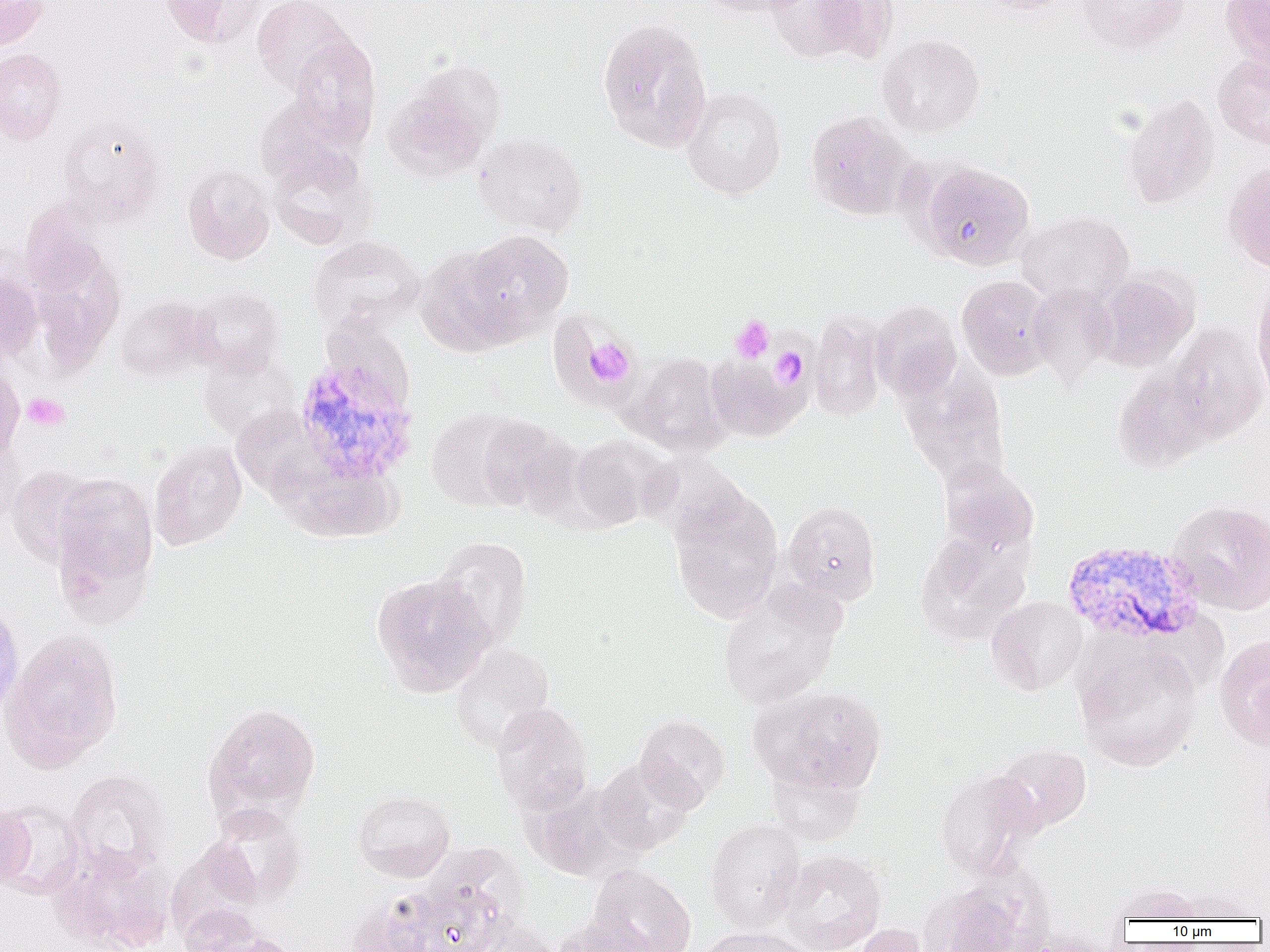
Summary:
  - Coordinate format: approximate bounding boxes as named x1/y1/x2/y2 corners in pixels
  - Plasmodium vivax-infected red blood cell locations: (x1=292, y1=354, x2=418, y2=486), (x1=1061, y1=540, x2=1205, y2=646)
  - Uninfected red blood cell locations: (x1=0, y1=0, x2=50, y2=51), (x1=158, y1=0, x2=265, y2=48), (x1=251, y1=0, x2=356, y2=93), (x1=695, y1=0, x2=810, y2=17), (x1=767, y1=0, x2=885, y2=62), (x1=978, y1=0, x2=1071, y2=14), (x1=1078, y1=0, x2=1189, y2=52), (x1=1220, y1=0, x2=1270, y2=70), (x1=598, y1=20, x2=712, y2=151), (x1=878, y1=34, x2=983, y2=135), (x1=288, y1=35, x2=380, y2=144), (x1=0, y1=48, x2=68, y2=145), (x1=1212, y1=55, x2=1270, y2=148), (x1=384, y1=67, x2=501, y2=182), (x1=683, y1=87, x2=786, y2=198), (x1=1123, y1=94, x2=1219, y2=208), (x1=256, y1=95, x2=361, y2=187), (x1=806, y1=111, x2=913, y2=219), (x1=56, y1=116, x2=165, y2=224), (x1=473, y1=135, x2=587, y2=235), (x1=268, y1=145, x2=373, y2=250), (x1=1223, y1=161, x2=1270, y2=275), (x1=918, y1=162, x2=1034, y2=269), (x1=182, y1=164, x2=275, y2=264), (x1=1018, y1=212, x2=1134, y2=306), (x1=461, y1=230, x2=573, y2=336), (x1=308, y1=236, x2=423, y2=331), (x1=25, y1=243, x2=126, y2=376), (x1=416, y1=247, x2=522, y2=355), (x1=0, y1=268, x2=44, y2=369), (x1=1095, y1=272, x2=1197, y2=371), (x1=957, y1=275, x2=1054, y2=380), (x1=1251, y1=279, x2=1270, y2=403), (x1=1027, y1=283, x2=1118, y2=378), (x1=189, y1=289, x2=283, y2=378), (x1=116, y1=297, x2=212, y2=380), (x1=870, y1=302, x2=962, y2=401), (x1=809, y1=315, x2=886, y2=420), (x1=1165, y1=323, x2=1268, y2=442), (x1=199, y1=351, x2=299, y2=441), (x1=625, y1=353, x2=730, y2=455), (x1=706, y1=356, x2=805, y2=440), (x1=0, y1=363, x2=24, y2=464), (x1=901, y1=366, x2=1010, y2=486), (x1=1114, y1=367, x2=1215, y2=470), (x1=231, y1=407, x2=324, y2=498), (x1=427, y1=408, x2=528, y2=510), (x1=474, y1=416, x2=579, y2=515), (x1=0, y1=433, x2=27, y2=528), (x1=570, y1=435, x2=665, y2=528), (x1=149, y1=441, x2=247, y2=550), (x1=275, y1=457, x2=399, y2=541), (x1=940, y1=462, x2=1039, y2=556), (x1=6, y1=465, x2=99, y2=567), (x1=50, y1=472, x2=158, y2=603), (x1=669, y1=488, x2=784, y2=622), (x1=1167, y1=499, x2=1270, y2=614), (x1=783, y1=502, x2=880, y2=603), (x1=917, y1=532, x2=1031, y2=643), (x1=432, y1=537, x2=532, y2=647), (x1=370, y1=572, x2=496, y2=696), (x1=718, y1=586, x2=843, y2=709), (x1=987, y1=596, x2=1087, y2=694), (x1=0, y1=597, x2=24, y2=723), (x1=1, y1=629, x2=122, y2=773), (x1=1215, y1=633, x2=1270, y2=752), (x1=1076, y1=640, x2=1201, y2=771), (x1=450, y1=645, x2=553, y2=752), (x1=754, y1=687, x2=887, y2=797), (x1=203, y1=703, x2=321, y2=821), (x1=491, y1=703, x2=591, y2=813), (x1=635, y1=715, x2=729, y2=811), (x1=993, y1=744, x2=1092, y2=833), (x1=594, y1=760, x2=694, y2=854), (x1=766, y1=764, x2=864, y2=844), (x1=66, y1=770, x2=168, y2=876), (x1=935, y1=771, x2=1043, y2=879), (x1=527, y1=783, x2=633, y2=879), (x1=353, y1=790, x2=455, y2=882), (x1=0, y1=799, x2=86, y2=899), (x1=0, y1=803, x2=35, y2=892), (x1=206, y1=803, x2=305, y2=906), (x1=705, y1=818, x2=804, y2=931), (x1=50, y1=845, x2=176, y2=952), (x1=779, y1=852, x2=885, y2=952), (x1=586, y1=866, x2=697, y2=952), (x1=403, y1=876, x2=511, y2=952), (x1=920, y1=882, x2=1040, y2=952), (x1=1112, y1=883, x2=1204, y2=923), (x1=171, y1=888, x2=265, y2=951), (x1=1173, y1=889, x2=1260, y2=922), (x1=346, y1=892, x2=442, y2=952), (x1=555, y1=915, x2=659, y2=951), (x1=466, y1=916, x2=561, y2=952), (x1=853, y1=924, x2=933, y2=952), (x1=698, y1=927, x2=814, y2=952), (x1=207, y1=933, x2=303, y2=952)
  - Platelet locations: (x1=731, y1=315, x2=775, y2=363), (x1=582, y1=337, x2=636, y2=389), (x1=771, y1=347, x2=808, y2=387), (x1=22, y1=393, x2=69, y2=431)
  - Slide-level diagnosis: Plasmodium vivax
  - Modality: optical microscopy
  - Field of view: single
  - Preparation: thin blood film
  - Image size: 1270×952 pixels
  - Magnification: 1000x